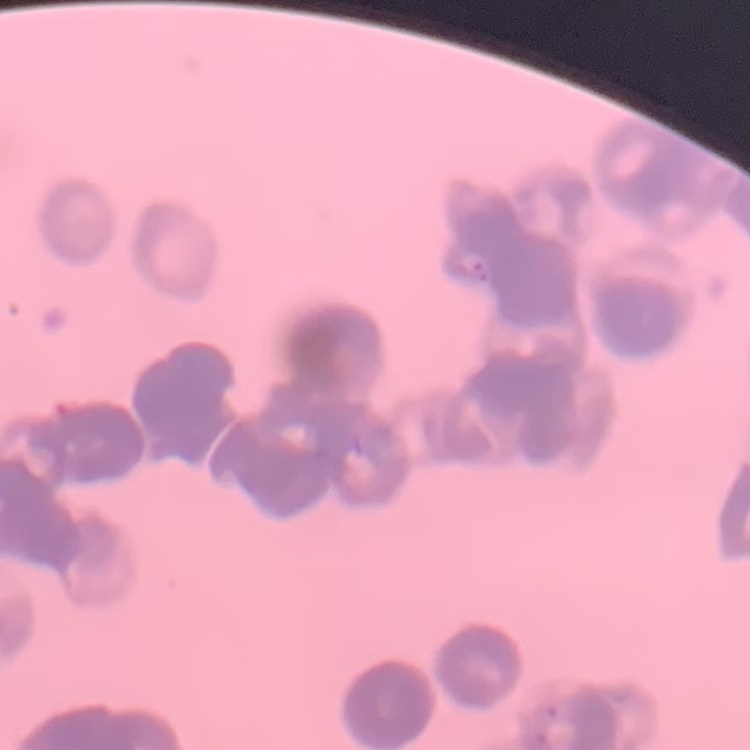
red blood cell morphology = rouleaux formation
preparation = thin blood smear
image type = one tile cut from a larger photomicrograph
stain = Field's or Giemsa